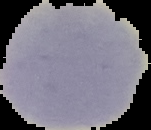

Image is 151×130 pixels. From a thin blood smear. The area outside the segmented cell region is set to black. Result: no malaria parasites detected.